Comment on the morphology of the erythrocytes.
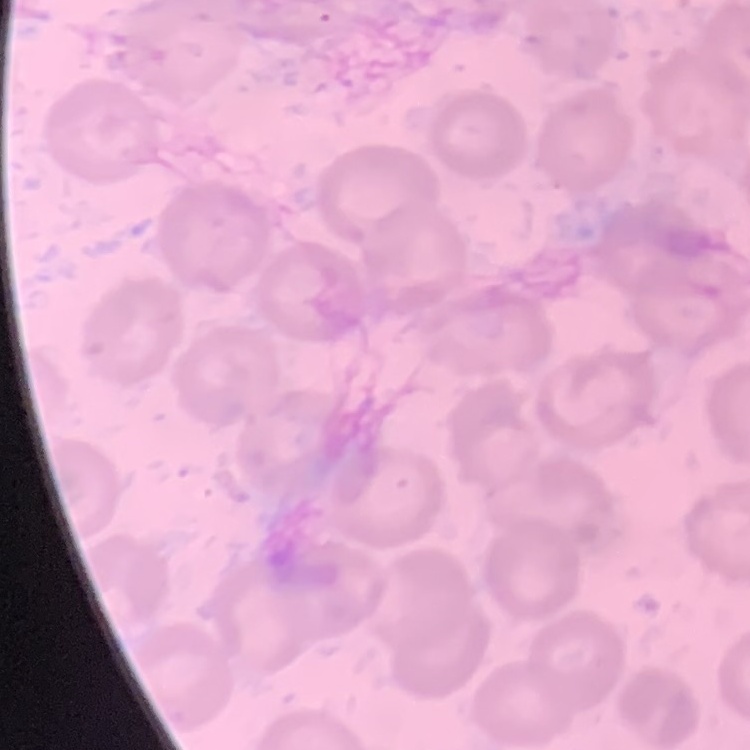

They show no rouleaux formation.

Summary:
  - Preparation: thin blood film
  - Image type: one tile cut from a larger photomicrograph
  - Stain: Field's or Giemsa